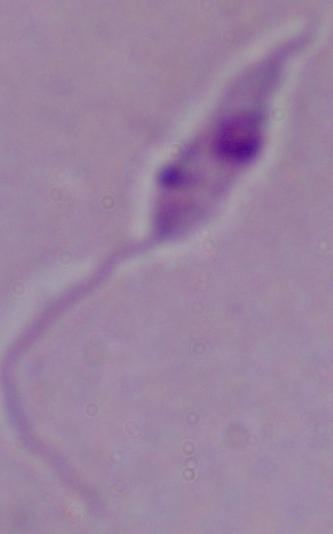
Summary:
  - Modality: micrograph
  - Identification: Leishmania
  - Magnification: 1000x